Assess this cell for malaria.
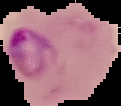

Parasitized.

Summary:
  - Image type: segmented cell region on a black background
  - Preparation: thin blood smear
  - Image size: 121×106 pixels